Describe the morphology of the erythrocytes.
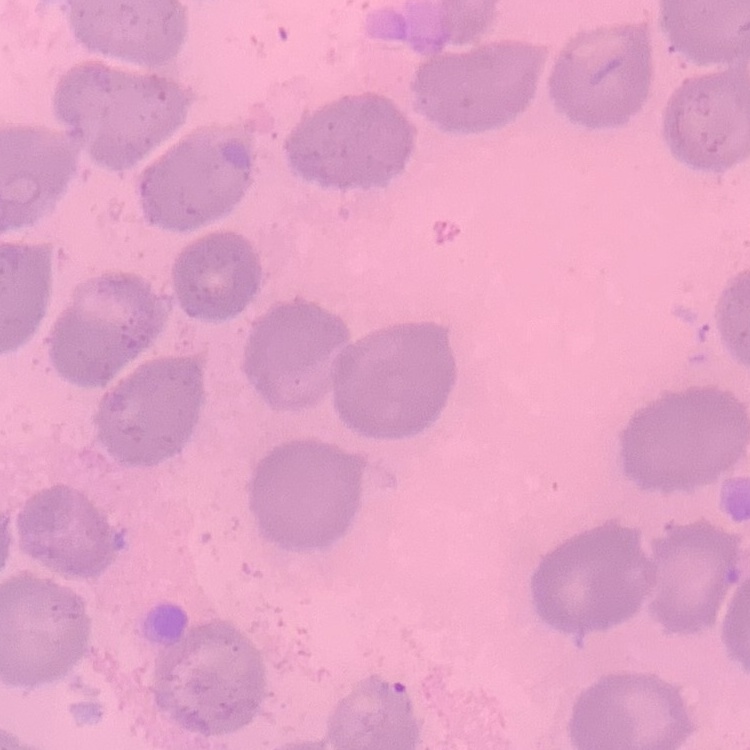

No rouleaux formation.

One tile cut from a larger photomicrograph. Thin blood film. Stained with either Field's or Giemsa.